Report the malaria status.
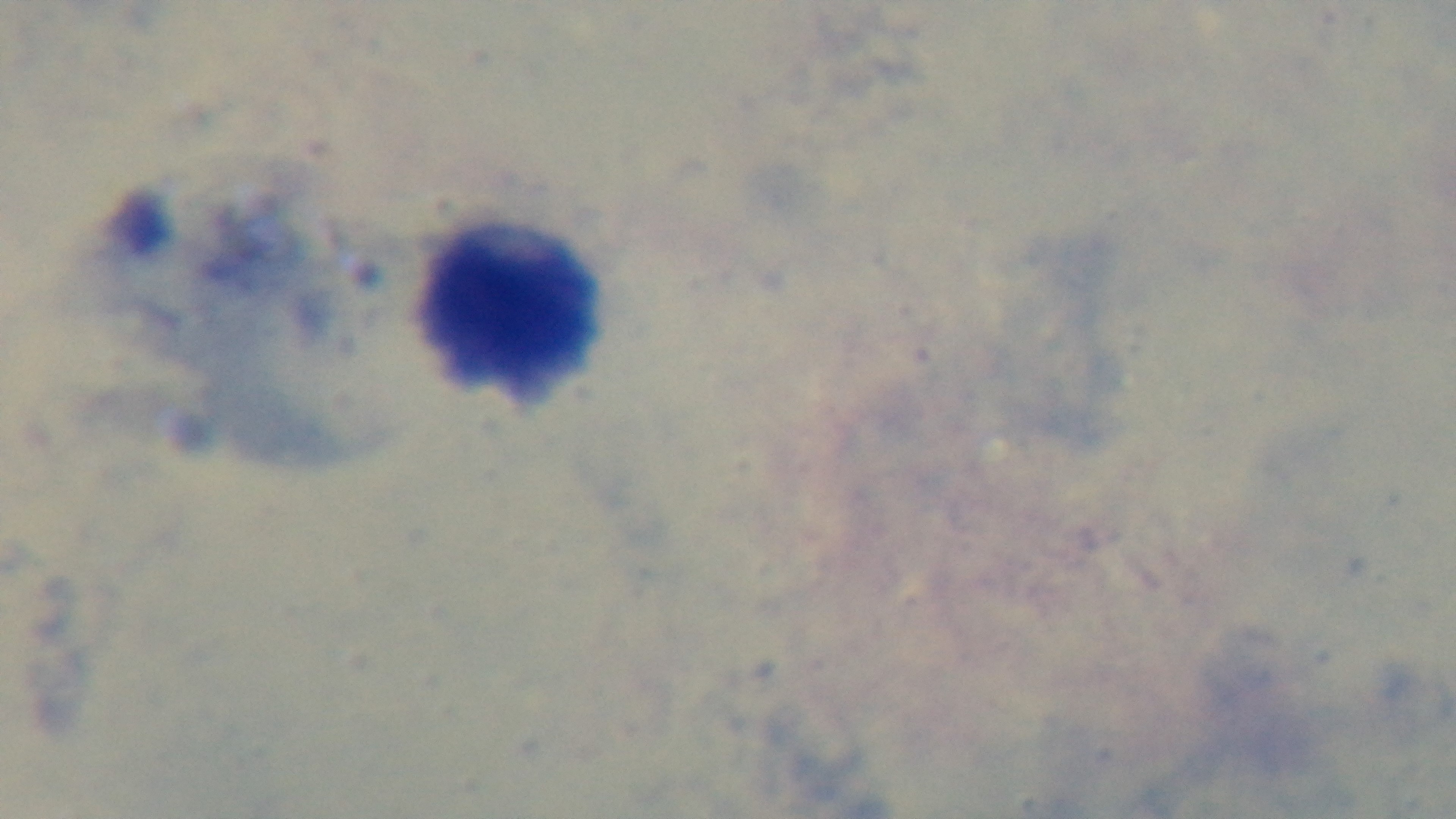
Negative.

modality: light microscopy
capture: mounted 4K digital camera
field_of_view: single
preparation: thick blood film
objective: 100x oil immersion
stain: Giemsa